Mark where platelets are.
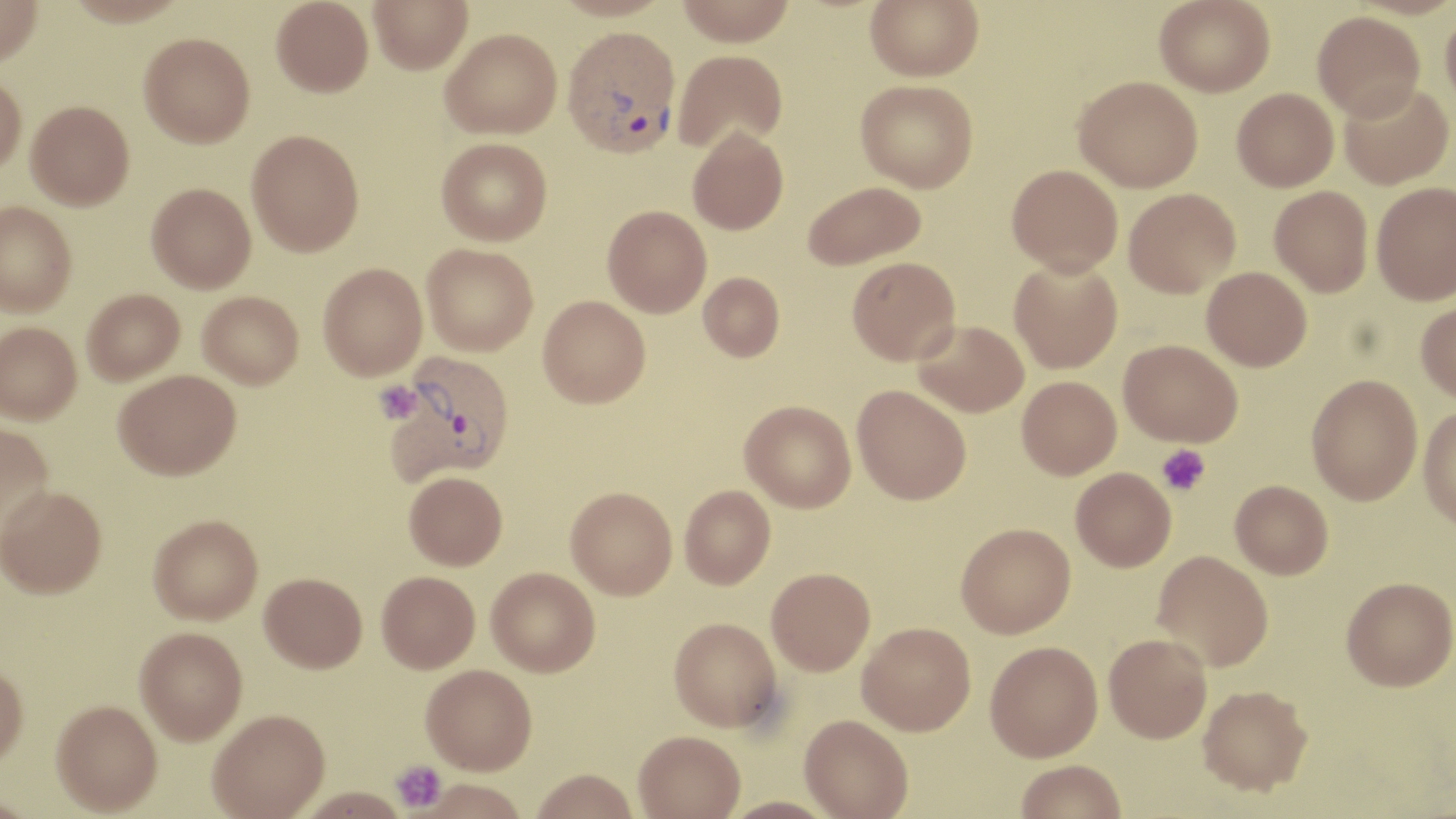

Approximate bounding boxes as [x1, y1, x2, y2] in pixels.
Platelets: [374, 381, 420, 422], [1156, 444, 1210, 497], [390, 759, 446, 815].

plasmodium_vivax_infected_red_blood_cell_locations: 'approximate bounding boxes as [x1, y1, x2, y2] in pixels: [562, 25, 681, 158], [384, 351, 515, 484]'
slide_level_diagnosis: Plasmodium vivax
field_of_view: one of a larger specimen
modality: light microscopy
image_size: 1456×819 pixels
preparation: thin blood film
uninfected_red_blood_cell_locations: 'approximate bounding boxes as [x1, y1, x2, y2] in pixels: [0, 0, 43, 67], [63, 0, 191, 26], [271, 0, 373, 97], [369, 0, 472, 74], [550, 0, 675, 21], [676, 0, 795, 46], [865, 0, 984, 81], [1154, 0, 1275, 97], [1441, 5, 1456, 112], [1313, 11, 1425, 121], [441, 28, 561, 139], [138, 33, 255, 147], [673, 49, 788, 153], [0, 72, 27, 179], [1074, 75, 1203, 192], [855, 79, 978, 192], [1339, 81, 1454, 189], [1232, 87, 1339, 191], [26, 100, 134, 210], [688, 127, 789, 235], [246, 129, 364, 256], [436, 137, 552, 245], [1007, 164, 1123, 276], [803, 180, 926, 269], [147, 182, 256, 293], [1371, 182, 1456, 304], [1269, 185, 1373, 297], [1124, 188, 1240, 297], [0, 201, 77, 315], [602, 205, 712, 317], [422, 243, 538, 355], [847, 256, 961, 365], [1009, 258, 1122, 374], [318, 262, 427, 380], [1202, 266, 1312, 370], [698, 271, 785, 361], [82, 288, 185, 385], [198, 291, 304, 389], [538, 295, 651, 407], [1416, 300, 1456, 403], [912, 319, 1029, 417], [1, 321, 82, 424], [1119, 339, 1242, 447], [113, 369, 240, 479], [1306, 374, 1423, 505], [1017, 376, 1121, 479], [852, 384, 971, 504], [740, 400, 856, 512], [1418, 406, 1456, 530], [0, 423, 54, 538], [1071, 467, 1176, 572], [404, 471, 507, 570], [1230, 480, 1333, 579], [0, 484, 106, 598], [680, 485, 775, 588], [566, 486, 677, 599], [149, 514, 264, 624], [956, 522, 1076, 638], [1152, 550, 1273, 671], [486, 567, 600, 676], [766, 567, 875, 675], [376, 570, 480, 672], [260, 572, 367, 672], [1341, 576, 1456, 690], [669, 616, 783, 733], [858, 622, 976, 735], [135, 627, 247, 744], [1104, 633, 1212, 743], [985, 641, 1103, 761], [0, 662, 28, 768], [421, 664, 537, 774], [1198, 684, 1313, 795], [51, 700, 163, 815], [208, 709, 329, 818], [799, 714, 914, 818], [633, 730, 745, 819], [1015, 759, 1126, 819], [530, 769, 639, 819], [294, 788, 412, 818], [720, 796, 839, 819]'
stain: May-Grünwald-Giemsa
magnification: 1000x